Point out each Plasmodium parasite and each leukocyte.
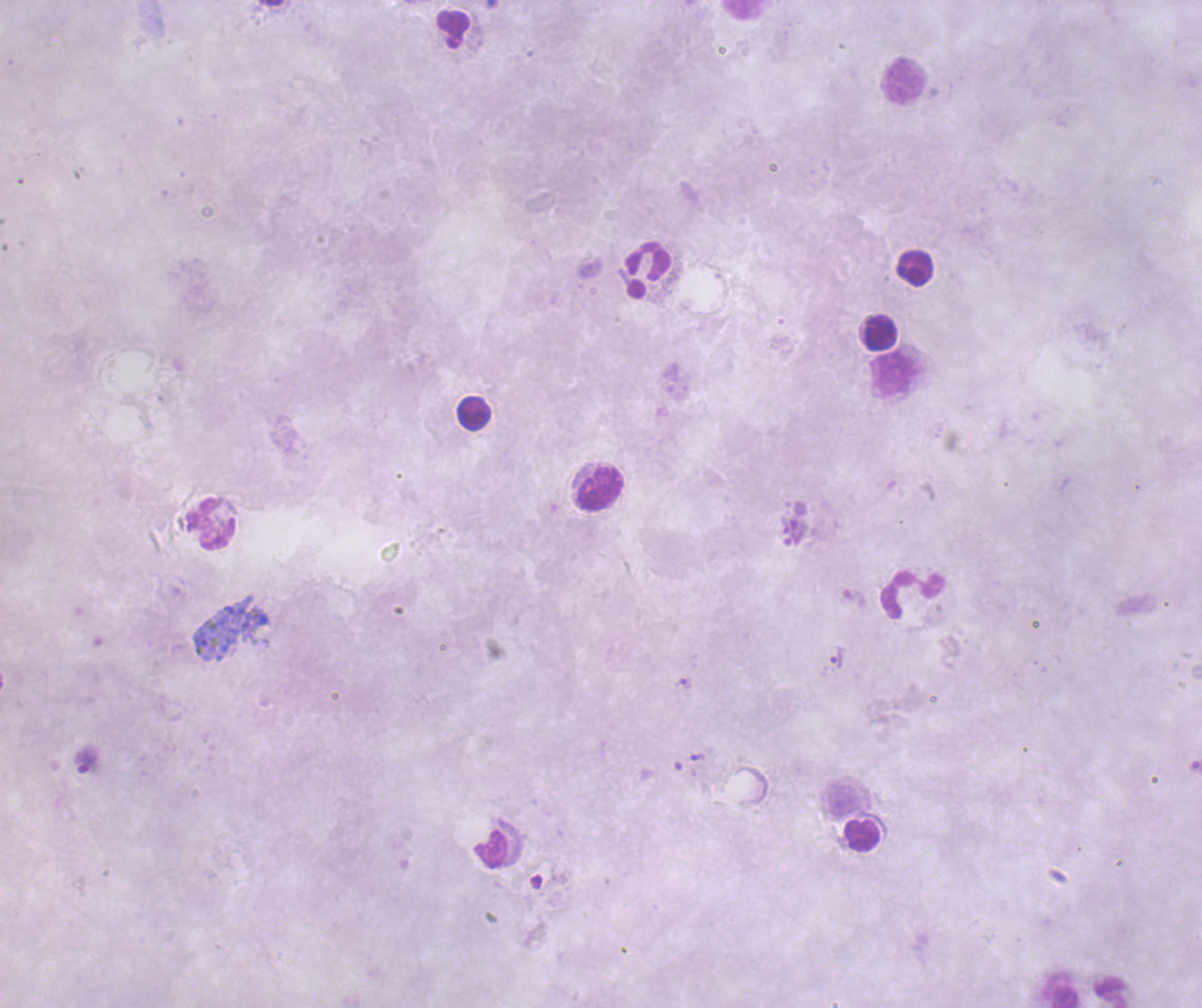
Approximate centers as (x, y) in pixels.
Trophozoites: (856, 599), (837, 657), (686, 683), (698, 757), (88, 761).
No schizont or gametocyte forms observed.
Leukocytes: (744, 10), (454, 29), (902, 80), (915, 268), (648, 269), (881, 332), (895, 375), (474, 413), (599, 489), (211, 524), (912, 594), (863, 835), (1062, 990).

coloration quality = bad
context = previously used in an actual diagnosis
background quality = unsatisfactory
field of view = one from this slide
magnification = 100x
preparation = thick blood smear
image size = 1202×1008 pixels
stain = Romanowsky